Outline every Plasmodium parasite, every leukocyte, and every artifact (stain precipitate or debris).
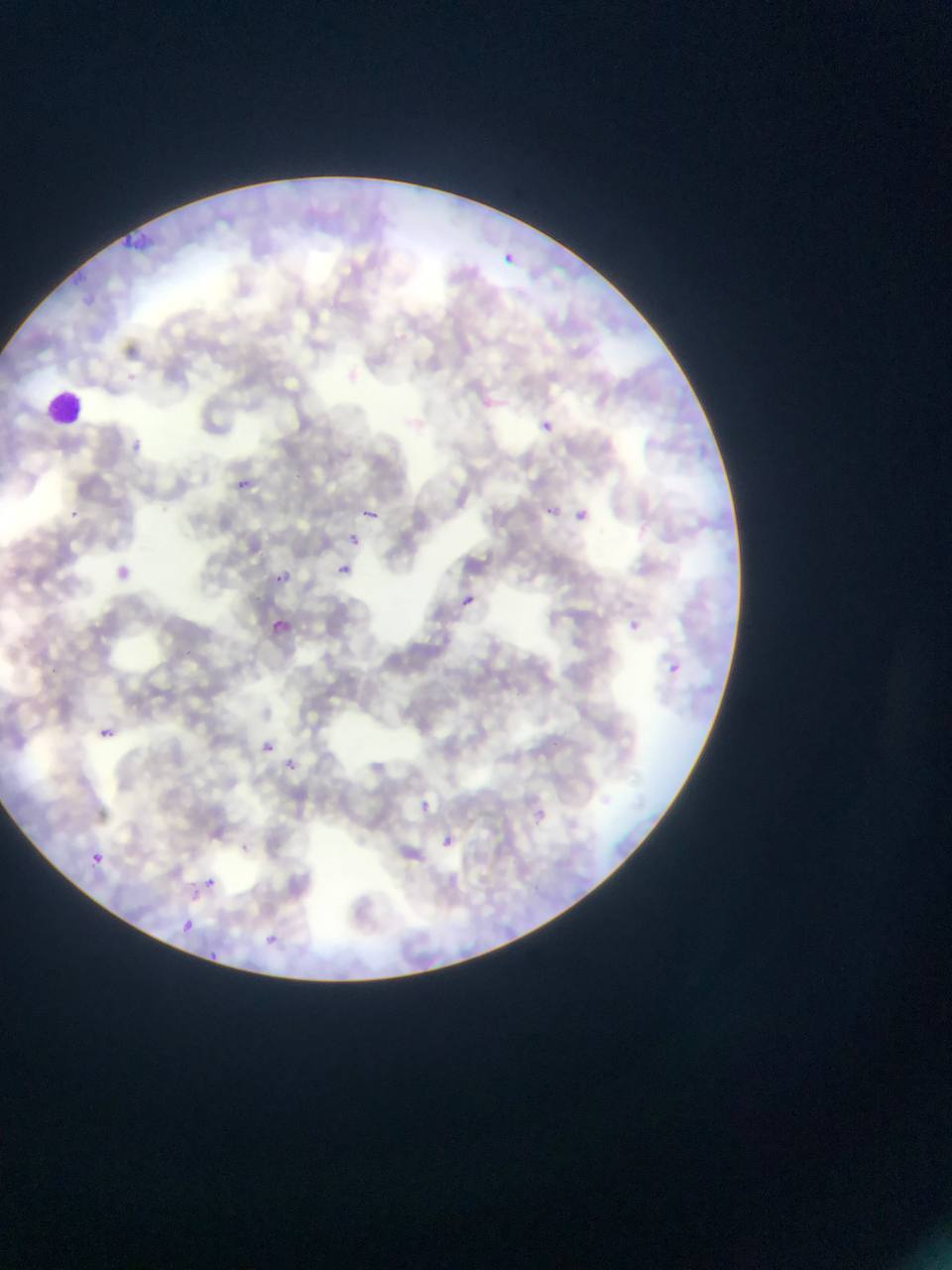

Approximate bounding boxes as [left, top, right, bottom] in pixels.
Plasmodium parasites: [505, 253, 516, 264], [480, 396, 496, 410], [541, 420, 554, 433], [125, 433, 142, 454], [230, 476, 253, 493], [65, 505, 81, 525], [545, 506, 556, 516], [365, 509, 378, 520], [577, 509, 589, 521], [348, 534, 361, 547], [116, 561, 132, 584], [340, 564, 352, 575], [277, 566, 291, 587], [463, 596, 475, 606], [270, 619, 287, 640], [670, 664, 680, 673], [100, 727, 113, 737], [262, 738, 275, 760], [282, 757, 305, 782], [416, 800, 431, 812], [536, 800, 552, 822], [533, 807, 549, 824], [440, 834, 456, 850], [91, 853, 104, 865], [204, 877, 218, 888], [180, 919, 195, 936], [259, 928, 281, 949], [210, 943, 222, 965].
Leukocytes: [45, 391, 84, 427].

capture: mobile-phone photograph through a microscope
preparation: thin blood film
country: Ghana
image_size: 952×1270 pixels
field_of_view: single